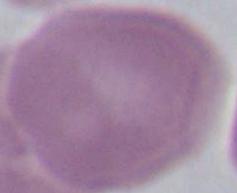

Summary:
  - Identification: erythrocyte
  - Magnification: 1000x
  - Modality: photomicrograph